Assess the morphology of the red blood cells.
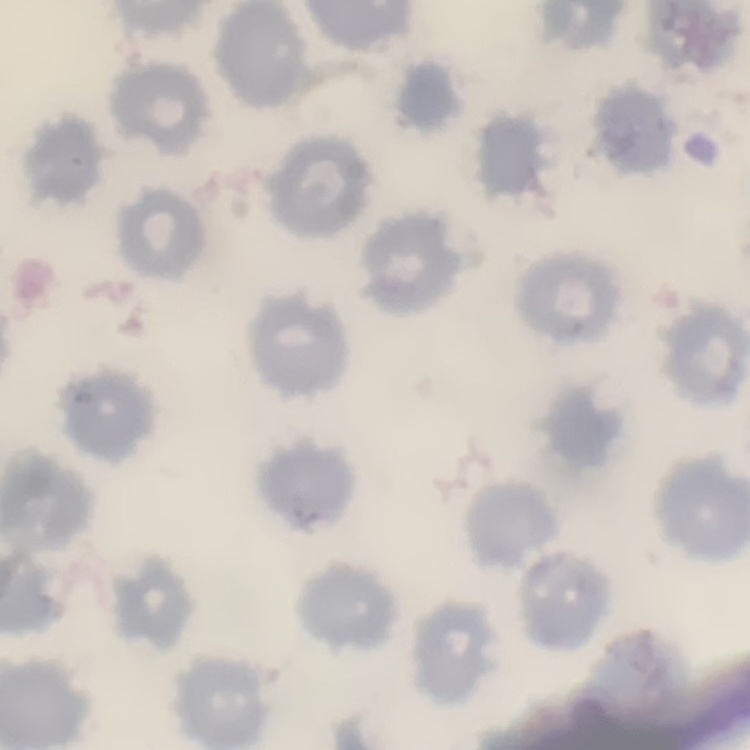
They show no rouleaux formation.

{
  "image_type": "one tile cut from a larger photomicrograph",
  "stain": "Field's or Giemsa",
  "preparation": "thin peripheral smear"
}